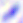
Summary:
  - Magnification: 400x
  - Identification: Toxoplasma gondii
  - Modality: photomicrograph